Give a bounding box for every malaria parasite.
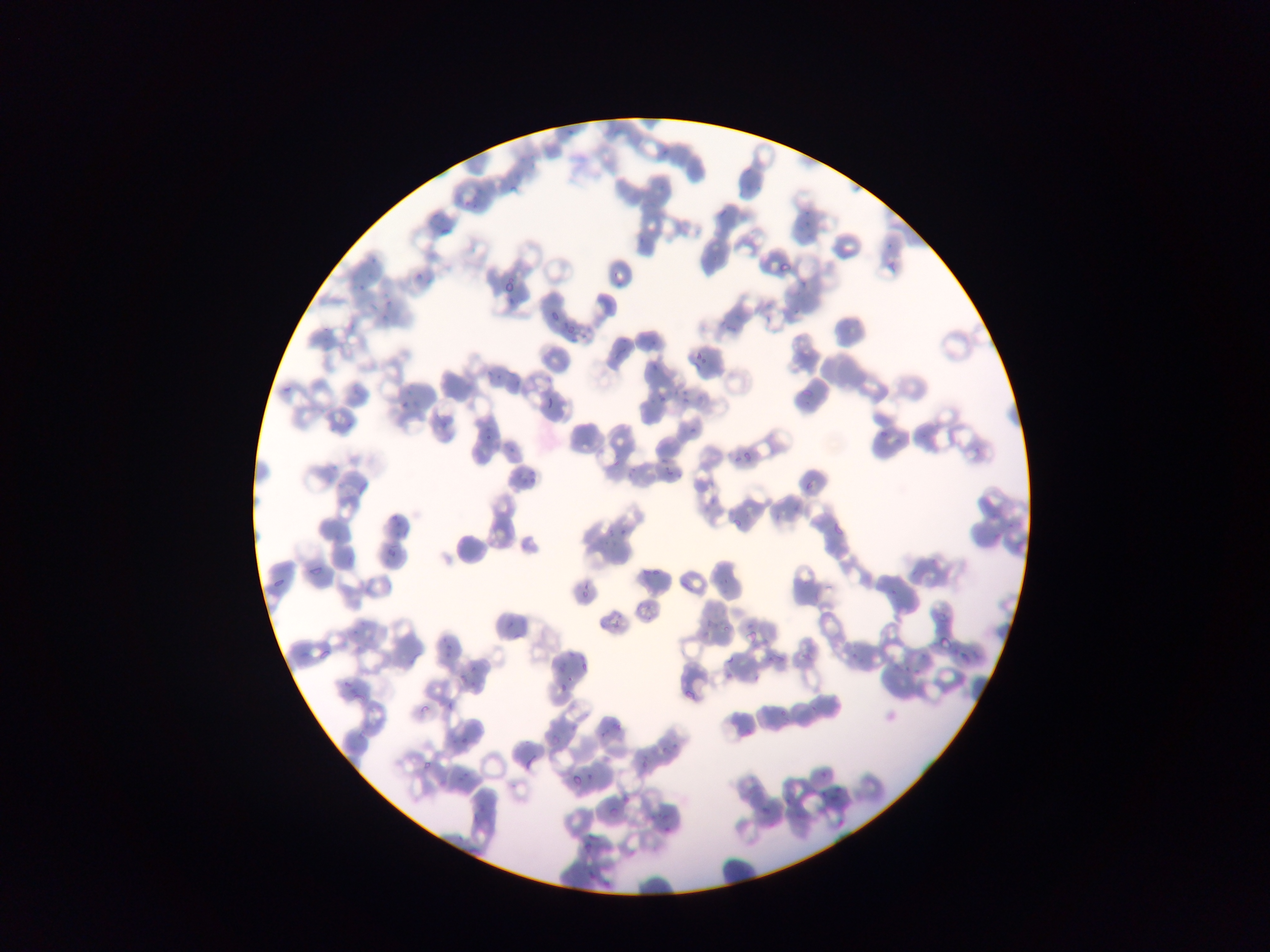

Approximate bounding boxes as {left, top, right, bottom} in pixels.
Malaria parasites: {563, 123, 582, 145}, {654, 141, 681, 159}, {506, 172, 532, 191}, {467, 188, 487, 214}, {799, 203, 820, 229}, {428, 213, 460, 241}, {369, 241, 383, 269}, {412, 271, 421, 280}, {356, 280, 367, 292}, {798, 281, 807, 290}, {505, 295, 516, 306}, {382, 298, 397, 309}, {546, 312, 558, 322}, {378, 314, 386, 323}, {562, 322, 574, 341}, {605, 342, 629, 358}, {692, 349, 707, 368}, {647, 366, 659, 378}, {493, 374, 507, 387}, {797, 384, 817, 403}, {281, 386, 291, 400}, {542, 391, 554, 412}, {678, 391, 695, 406}, {655, 393, 664, 406}, {397, 395, 414, 415}, {428, 418, 459, 439}, {880, 425, 888, 435}, {688, 427, 697, 439}, {479, 432, 493, 449}, {504, 447, 514, 453}, {733, 451, 751, 464}, {509, 467, 544, 489}, {659, 468, 676, 475}, {804, 476, 815, 494}, {792, 500, 801, 509}, {389, 511, 404, 531}, {735, 517, 741, 526}, {620, 523, 632, 538}, {602, 524, 616, 536}, {835, 524, 847, 539}, {596, 540, 605, 550}, {381, 546, 392, 560}, {309, 554, 330, 574}, {906, 564, 933, 579}, {259, 567, 294, 588}, {639, 572, 656, 579}, {575, 574, 596, 602}, {885, 575, 909, 596}, {715, 576, 739, 592}, {634, 595, 653, 622}, {602, 611, 625, 636}, {740, 618, 755, 646}, {499, 620, 518, 642}, {720, 623, 729, 633}, {441, 628, 460, 658}, {950, 634, 968, 653}, {316, 637, 341, 658}, {962, 647, 971, 659}, {802, 648, 816, 657}, {759, 650, 778, 667}, {558, 654, 581, 697}, {903, 655, 926, 672}, {571, 656, 592, 677}, {845, 657, 854, 667}, {725, 658, 738, 670}, {459, 667, 476, 691}, {341, 683, 367, 708}, {445, 689, 466, 714}, {680, 689, 701, 717}, {414, 700, 429, 721}, {777, 706, 794, 729}, {600, 719, 622, 738}, {357, 720, 373, 745}, {452, 731, 474, 760}, {660, 737, 681, 756}, {523, 744, 542, 777}, {416, 751, 445, 772}, {579, 765, 595, 783}, {453, 771, 475, 790}, {819, 772, 828, 785}, {782, 778, 816, 807}, {570, 780, 585, 789}, {832, 781, 854, 800}, {606, 785, 641, 817}, {743, 788, 754, 796}, {760, 792, 788, 816}, {818, 794, 829, 804}, {790, 805, 808, 827}, {467, 809, 494, 826}, {646, 813, 654, 826}, {664, 816, 675, 833}, {835, 816, 845, 827}, {574, 834, 591, 854} | approximate {x, y} pixel centers of objects too small to bound: {777, 516}, {644, 764}.

country = Ghana
preparation = thin blood film
capture = mobile-phone photograph through a microscope
image size = 1270×952 pixels
field of view = single